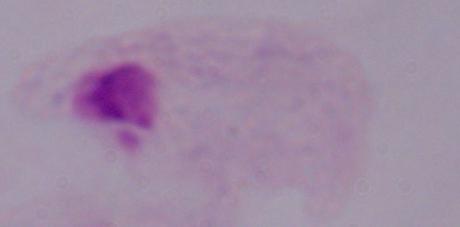
Summary:
  - Modality: photomicrograph
  - Magnification: 1000x
  - Identification: trichomonad